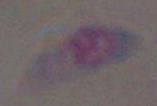
magnification: 1000x
identification: Toxoplasma gondii
modality: photomicrograph